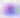
Toxoplasma gondii is shown. Micrograph. Captured at 400x magnification.